Name the blood parasite species.
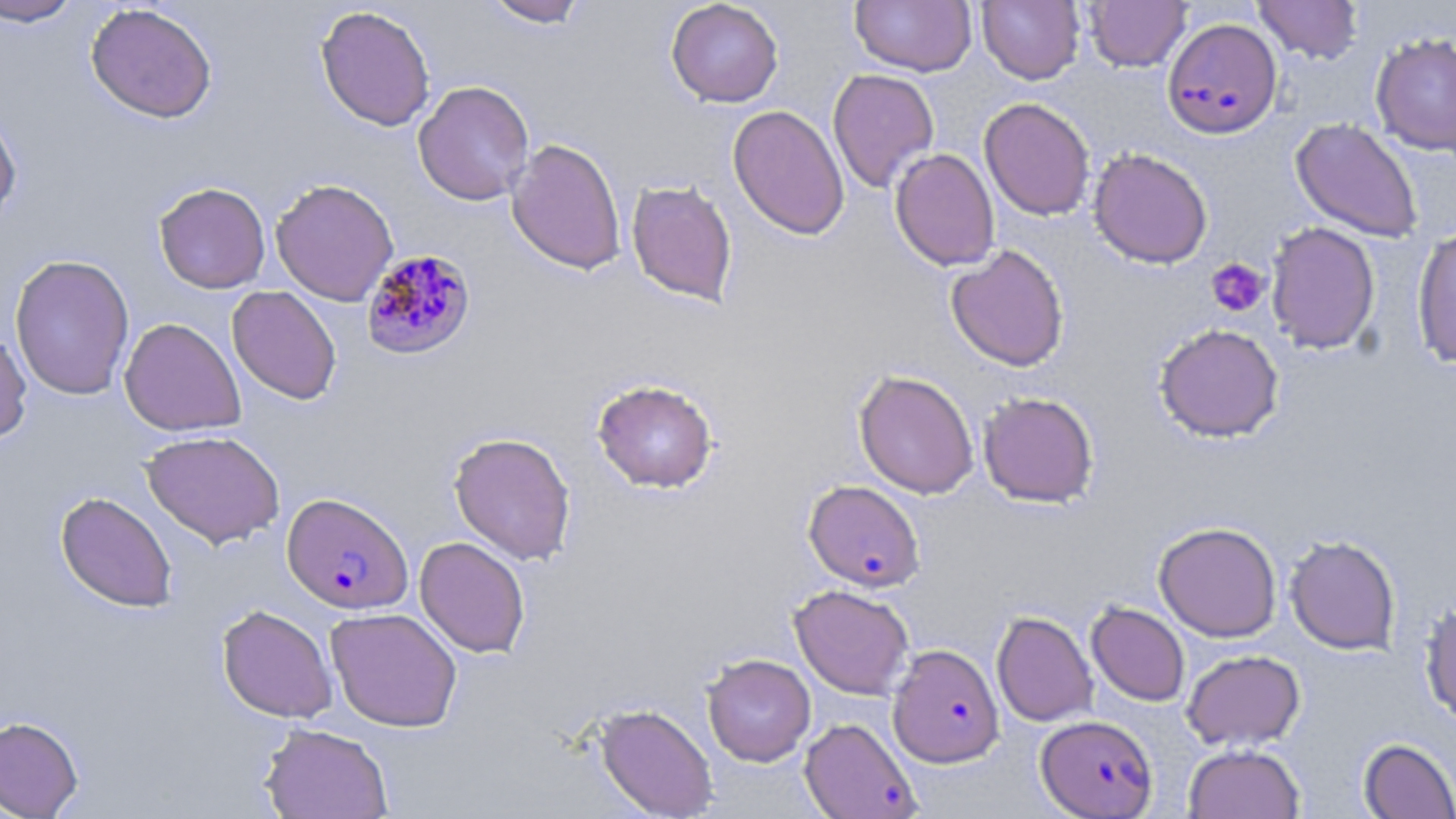
Plasmodium falciparum.

{
  "image_size": "1456×819 pixels",
  "magnification": "1000x",
  "uninfected_red_blood_cell_locations": "approximate bounding boxes as (x1, y1, x2, y2) in pixels: (0, 0, 84, 27), (483, 0, 589, 28), (665, 0, 783, 107), (850, 0, 976, 77), (977, 0, 1085, 85), (1084, 0, 1191, 73), (1252, 0, 1364, 65), (85, 3, 218, 123), (315, 5, 436, 131), (1370, 31, 1456, 156), (827, 68, 940, 194), (413, 80, 535, 206), (979, 97, 1095, 221), (0, 103, 22, 228), (727, 104, 850, 240), (1290, 118, 1423, 243), (506, 138, 627, 276), (1088, 147, 1213, 268), (890, 148, 1000, 271), (270, 178, 399, 306), (625, 178, 738, 306), (153, 181, 270, 294), (1266, 222, 1381, 354), (1412, 225, 1456, 369), (945, 244, 1070, 372), (9, 254, 135, 400), (227, 286, 342, 405), (119, 317, 245, 436), (1153, 323, 1284, 443), (0, 325, 32, 445), (853, 369, 979, 499), (592, 378, 718, 493), (978, 391, 1099, 507), (141, 429, 285, 548), (448, 431, 577, 566), (55, 491, 178, 612), (1153, 521, 1282, 642), (1285, 534, 1401, 655), (414, 536, 530, 658), (789, 584, 915, 699), (1419, 600, 1456, 726), (1086, 601, 1190, 706), (217, 604, 337, 723), (325, 607, 463, 732), (991, 610, 1098, 727), (1181, 649, 1306, 751), (702, 653, 816, 766), (594, 703, 718, 818), (0, 715, 83, 818), (259, 722, 394, 819), (1358, 737, 1456, 818), (1183, 743, 1305, 819)",
  "stain": "May-Grünwald-Giemsa",
  "plasmodium_falciparum_infected_red_blood_cell_locations": "approximate bounding boxes as (x1, y1, x2, y2) in pixels: (1162, 17, 1282, 139), (360, 250, 476, 360), (803, 479, 925, 592), (282, 492, 413, 614), (887, 643, 1004, 767), (1036, 715, 1158, 818), (800, 717, 921, 819)",
  "platelet_locations": "approximate bounding boxes as (x1, y1, x2, y2) in pixels: (1205, 258, 1270, 318)",
  "field_of_view": "one of a larger specimen",
  "preparation": "thin blood smear",
  "modality": "light microscopy"
}